Assess this cell for malaria.
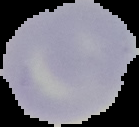

Uninfected.

preparation = thin blood smear
image type = segmented cell region with the area outside set to black
image size = 139×127 pixels